Classify this cell by malaria status.
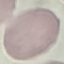
Uninfected.

Summary:
  - Capture: smartphone through the microscope eyepiece
  - Image type: cell patch, automatically extracted from a larger field of view and resized to 64 × 64 pixels
  - Stain: Giemsa
  - Preparation: thin blood smear